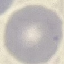
Summary:
  - Result: negative for malaria parasites
  - Preparation: thin blood film
  - Stain: Giemsa
  - Capture: smartphone camera at the microscope eyepiece
  - Image type: automatically extracted cell patch, resized to 64 × 64 pixels